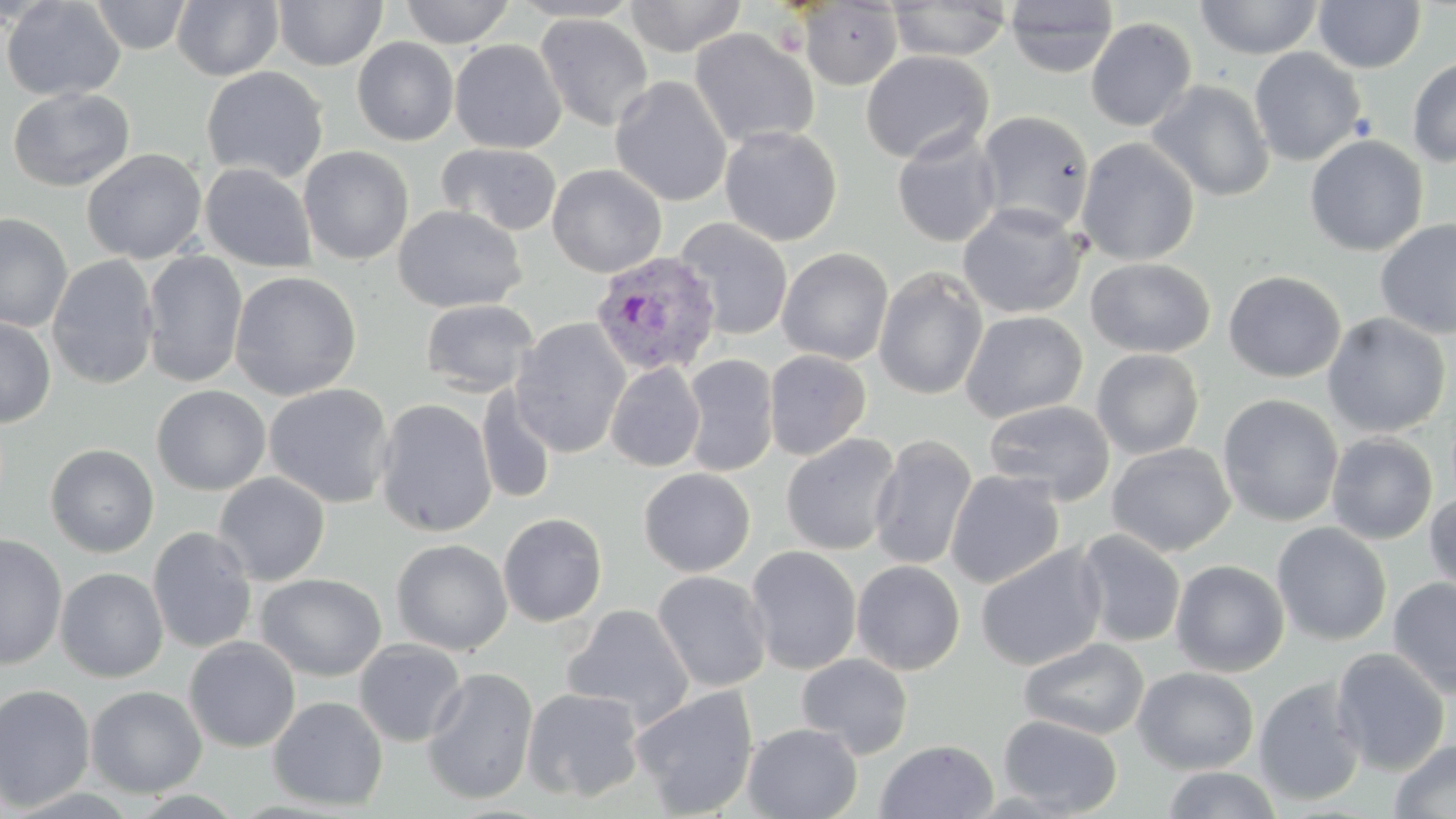
Plasmodium vivax-infected red blood cell locations = approximate bounding boxes as [x1, y1, x2, y2] in pixels: [590, 251, 722, 377]
slide-level diagnosis = Plasmodium vivax
magnification = 1000x
field of view = one of a larger specimen
modality = optical microscopy
uninfected red blood cell locations = approximate bounding boxes as [x1, y1, x2, y2] in pixels: [1, 0, 125, 102], [90, 0, 192, 55], [171, 0, 283, 81], [400, 0, 515, 47], [507, 0, 643, 22], [624, 0, 748, 57], [889, 0, 1011, 61], [273, 1, 388, 71], [798, 1, 904, 90], [1003, 1, 1119, 78], [1194, 1, 1324, 60], [1313, 1, 1425, 73], [535, 13, 654, 132], [1085, 17, 1198, 132], [689, 27, 819, 149], [352, 37, 459, 146], [449, 38, 567, 154], [1249, 47, 1367, 166], [861, 50, 993, 165], [1407, 56, 1456, 168], [201, 66, 329, 184], [609, 76, 732, 207], [1146, 79, 1275, 202], [7, 87, 134, 192], [976, 110, 1095, 234], [719, 124, 842, 246], [891, 132, 1002, 248], [1304, 134, 1428, 256], [1076, 137, 1200, 266], [436, 143, 563, 237], [298, 145, 414, 265], [82, 148, 207, 264], [200, 162, 318, 273], [547, 164, 667, 278], [957, 202, 1086, 319], [393, 204, 526, 313], [0, 212, 73, 332], [1374, 217, 1456, 339], [676, 218, 793, 340], [776, 247, 894, 365], [141, 251, 248, 388], [47, 255, 160, 390], [1084, 256, 1215, 358], [873, 266, 989, 401], [229, 270, 362, 401], [1223, 270, 1346, 382], [421, 298, 539, 397], [959, 310, 1088, 423], [1322, 313, 1451, 438], [0, 316, 56, 428], [510, 317, 631, 458], [1091, 348, 1205, 460], [764, 350, 871, 460], [682, 354, 778, 477], [605, 362, 705, 472], [263, 383, 395, 508], [152, 385, 271, 496], [476, 386, 557, 506], [1217, 394, 1344, 527], [374, 398, 498, 538], [983, 400, 1116, 506], [780, 433, 902, 556], [1326, 433, 1438, 545], [869, 435, 978, 570], [1106, 442, 1236, 557], [45, 444, 159, 558], [639, 467, 756, 577], [944, 470, 1065, 588], [213, 472, 330, 586], [1424, 490, 1456, 602], [497, 512, 607, 627], [1272, 522, 1393, 646], [147, 526, 258, 654], [1074, 529, 1186, 648], [0, 533, 67, 670], [391, 538, 512, 655], [975, 544, 1106, 671], [746, 545, 862, 675], [1171, 559, 1290, 677], [851, 560, 965, 675], [55, 567, 169, 682], [651, 570, 772, 693], [255, 573, 387, 681], [1388, 576, 1456, 699], [561, 604, 694, 728], [184, 636, 301, 753], [1018, 637, 1150, 740], [354, 639, 467, 747], [1330, 647, 1450, 776], [796, 652, 913, 759], [1132, 666, 1260, 775], [422, 667, 538, 804], [1252, 677, 1367, 807], [0, 683, 96, 812], [85, 686, 207, 798], [629, 686, 759, 817], [522, 687, 646, 803], [268, 696, 388, 811], [998, 714, 1122, 816], [742, 723, 863, 818], [1388, 739, 1456, 819], [875, 740, 998, 819], [1161, 767, 1285, 819]
stain = May-Grünwald-Giemsa
image size = 1456×819 pixels
preparation = thin blood smear